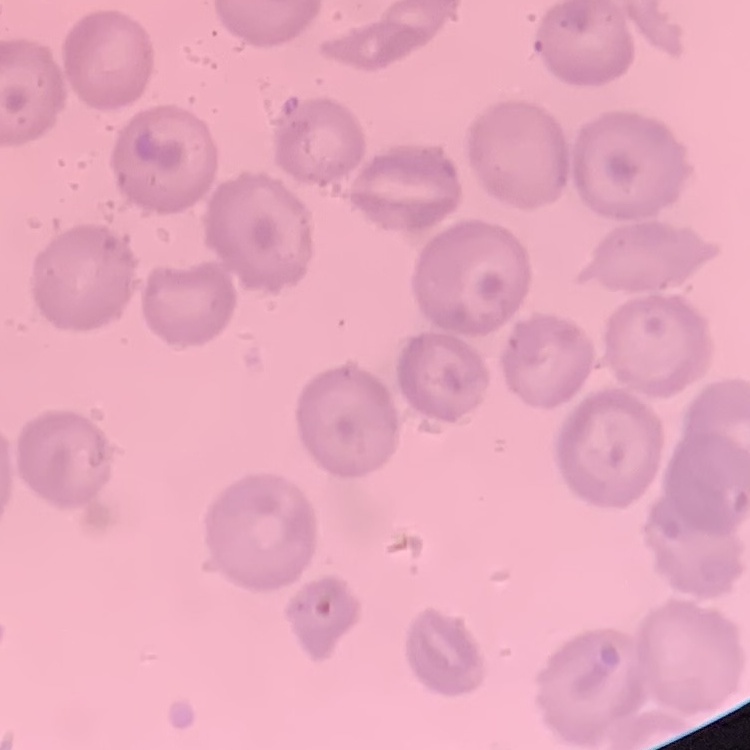

Summary:
  - Erythrocyte morphology: no rouleaux formation
  - Stain: Field's or Giemsa
  - Preparation: thin peripheral smear
  - Image type: one tile cut from a larger photomicrograph